Give the preparation type.
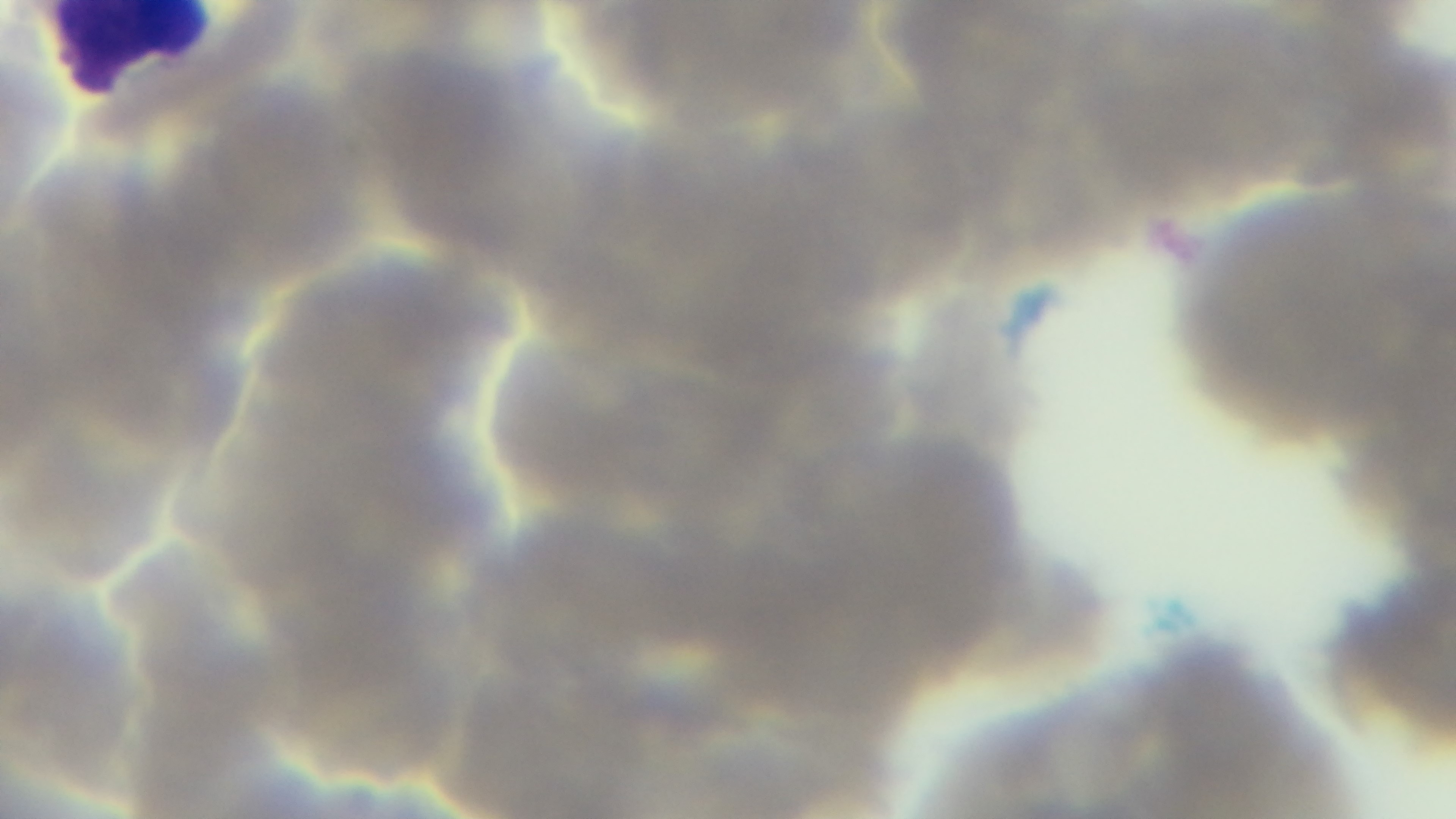
A thin smear.

objective = 100x oil immersion
field of view = one from the slide
capture = mounted 4K digital camera
modality = light microscopy
malaria status = positive
stain = Giemsa